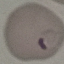

Malaria status: parasitized. Giemsa-stained preparation. Cell patch, automatically extracted from a larger field of view and resized to 64 × 64 pixels. Photographed with a smartphone camera at the microscope eyepiece. Thin blood smear.